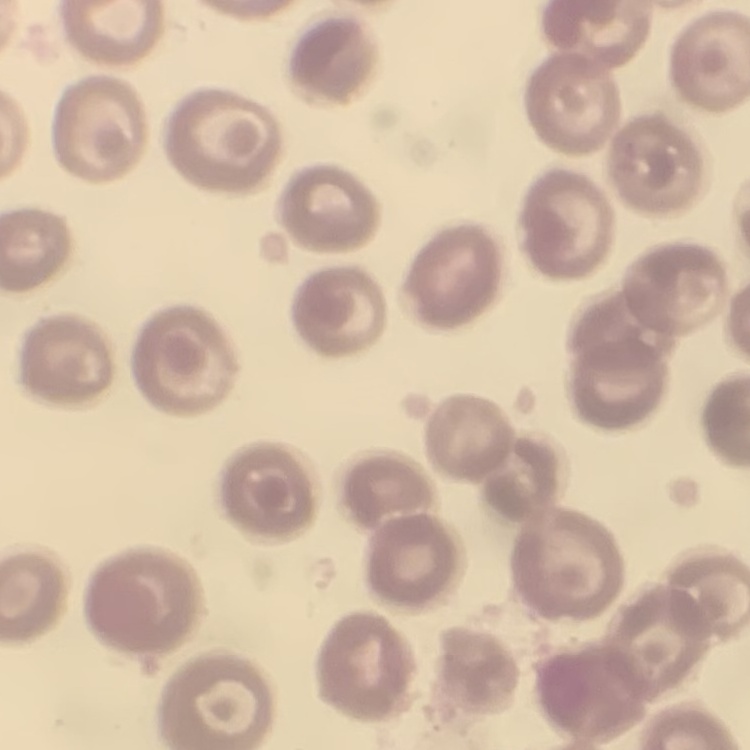
red blood cell morphology = no rouleaux formation
image type = square crop of a larger photomicrograph
stain = Field's or Giemsa
preparation = thin blood smear